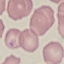 Result: negative for malaria parasites. Thin blood smear. Automatically extracted cell patch, resized to 64 × 64 pixels. Giemsa stain. Photographed with a smartphone camera at the microscope eyepiece.